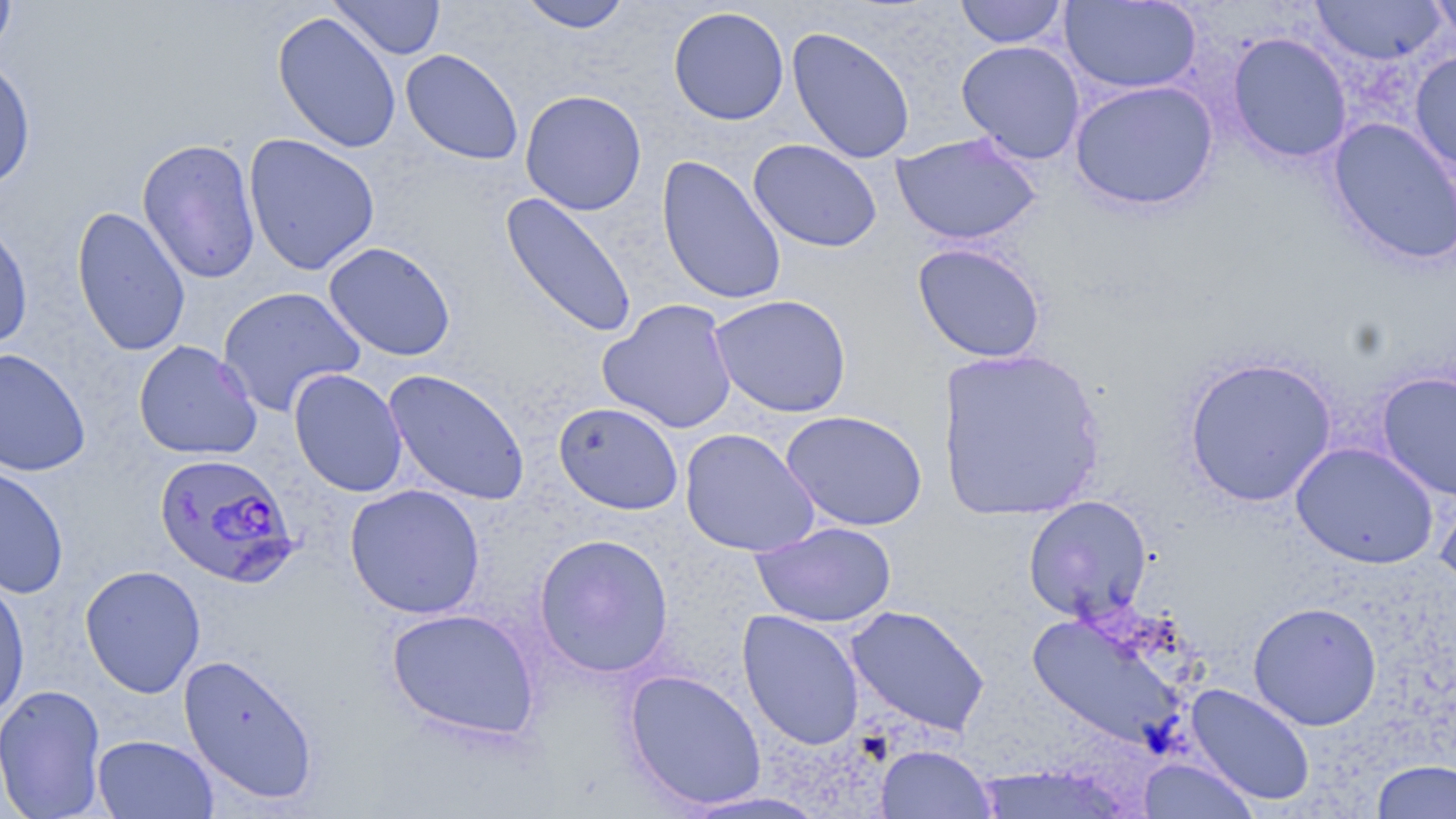
Approximate bounding boxes as [x1, y1, x2, y2] in pixels. Uninfected red blood cell locations: [0, 0, 17, 61], [329, 0, 446, 60], [517, 0, 634, 32], [954, 0, 1070, 48], [1060, 0, 1202, 95], [1310, 0, 1447, 65], [1426, 0, 1456, 45], [668, 6, 789, 125], [272, 11, 402, 154], [786, 26, 916, 165], [1226, 32, 1352, 164], [956, 40, 1086, 164], [400, 49, 523, 165], [1409, 50, 1456, 176], [0, 56, 36, 193], [1069, 80, 1220, 211], [520, 89, 647, 215], [1327, 117, 1456, 268], [890, 132, 1043, 246], [243, 133, 380, 276], [137, 138, 261, 285], [748, 139, 883, 253], [656, 154, 787, 307], [500, 193, 637, 339], [71, 205, 191, 357], [0, 216, 34, 352], [323, 241, 456, 361], [912, 242, 1047, 363], [216, 286, 366, 418], [709, 294, 852, 418], [598, 298, 738, 434], [133, 340, 263, 461], [0, 347, 91, 476], [934, 347, 1107, 522], [1182, 356, 1337, 507], [288, 368, 408, 497], [382, 368, 530, 506], [1376, 370, 1456, 502], [553, 401, 684, 515], [780, 409, 928, 532], [679, 428, 821, 557], [1291, 441, 1439, 569], [0, 463, 69, 599], [1435, 473, 1456, 597], [345, 484, 486, 619], [1022, 495, 1153, 622], [750, 521, 897, 627], [533, 532, 674, 678], [79, 564, 206, 698], [0, 573, 31, 724], [1248, 601, 1382, 730], [845, 604, 990, 737], [385, 607, 540, 741], [737, 609, 865, 751], [1027, 609, 1192, 752], [177, 653, 319, 806], [623, 669, 767, 810], [1, 684, 107, 819], [1185, 684, 1316, 807], [92, 734, 219, 818], [875, 744, 997, 819], [1137, 757, 1260, 819], [1370, 759, 1456, 818], [677, 789, 832, 818]. Plasmodium falciparum-infected red blood cell locations: [154, 452, 300, 587]. Slide-level diagnosis: Plasmodium falciparum. 1000x magnification. Thin blood smear. Optical microscopy. May-Grünwald-Giemsa stain. Image is 1456×819 pixels. One field of a larger specimen.